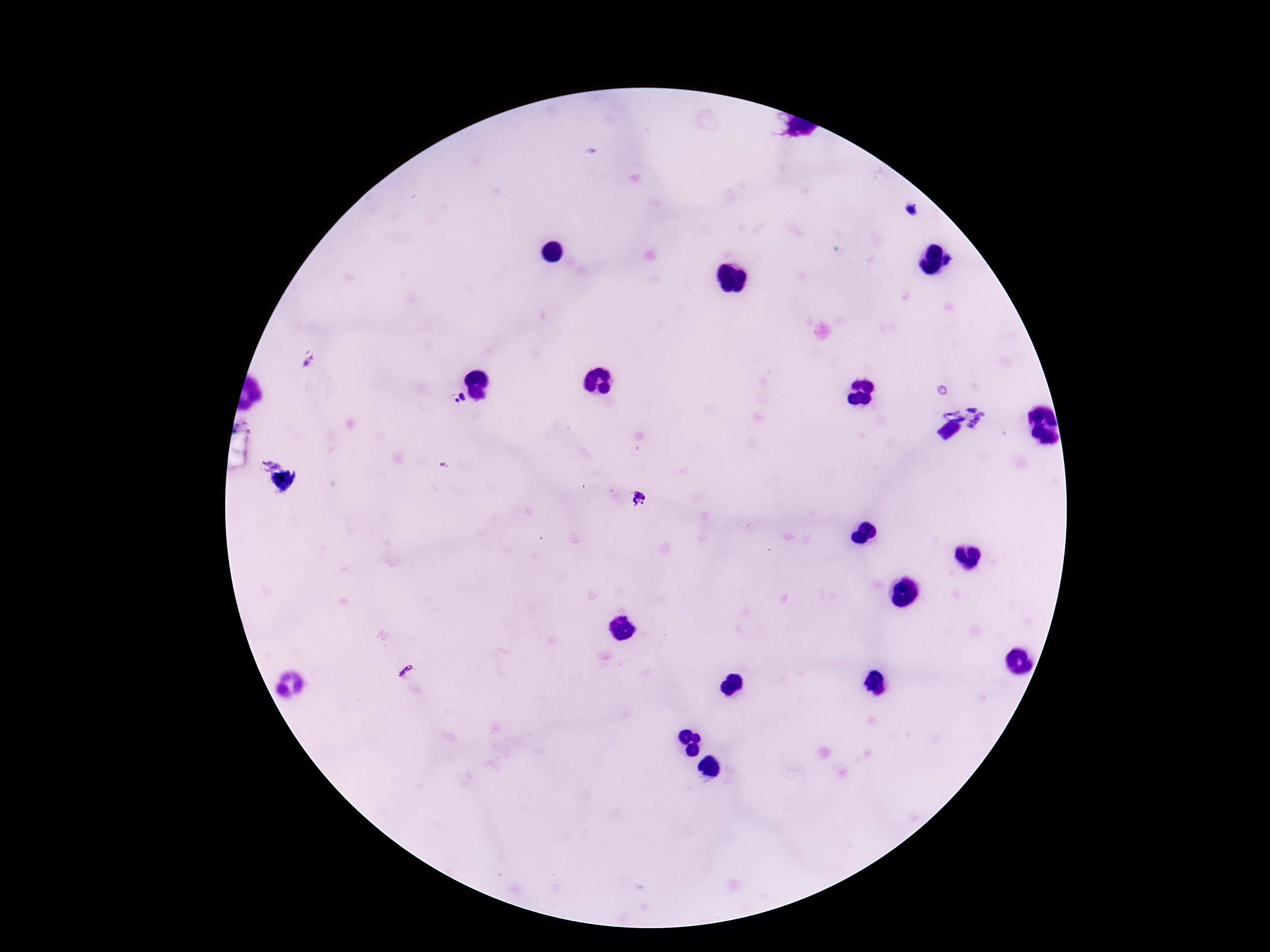
Approximate centers as (x, y) in pixels. Plasmodium parasite locations: (460, 397), (639, 499). Photographed through the microscope eyepiece with a smartphone camera. Giemsa stain. Thick blood smear. 100x magnification. Image is 1270×952 pixels. One field from this slide. Patient malaria status: infected.